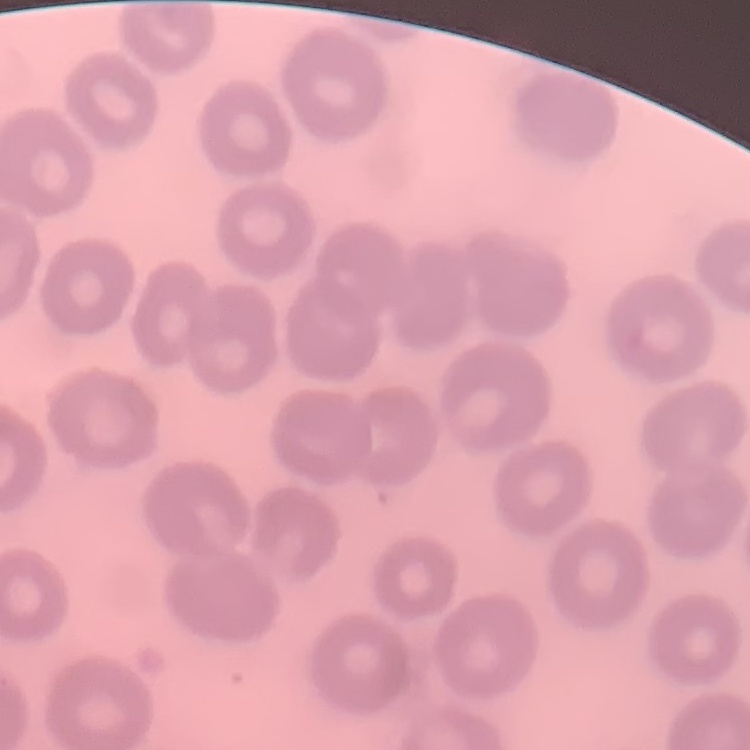
The erythrocytes exhibit no rouleaux formation. One tile cut from a larger photomicrograph. Field's or Giemsa stain. Thin blood smear.